Describe the morphology of the erythrocytes.
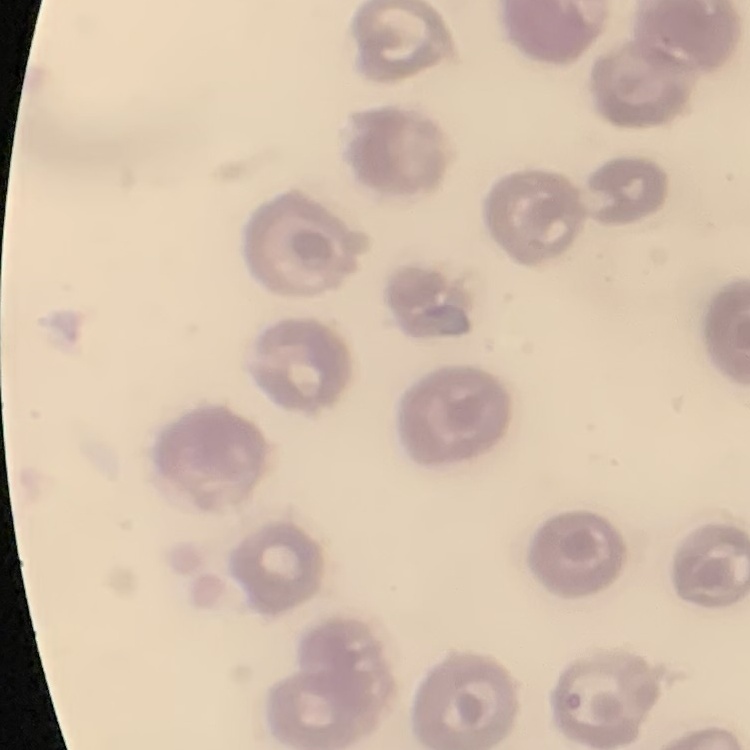
No rouleaux formation.

Summary:
  - Stain: Field's or Giemsa
  - Image type: one tile cut from a larger photomicrograph
  - Preparation: thin peripheral smear